Mark where platelets are.
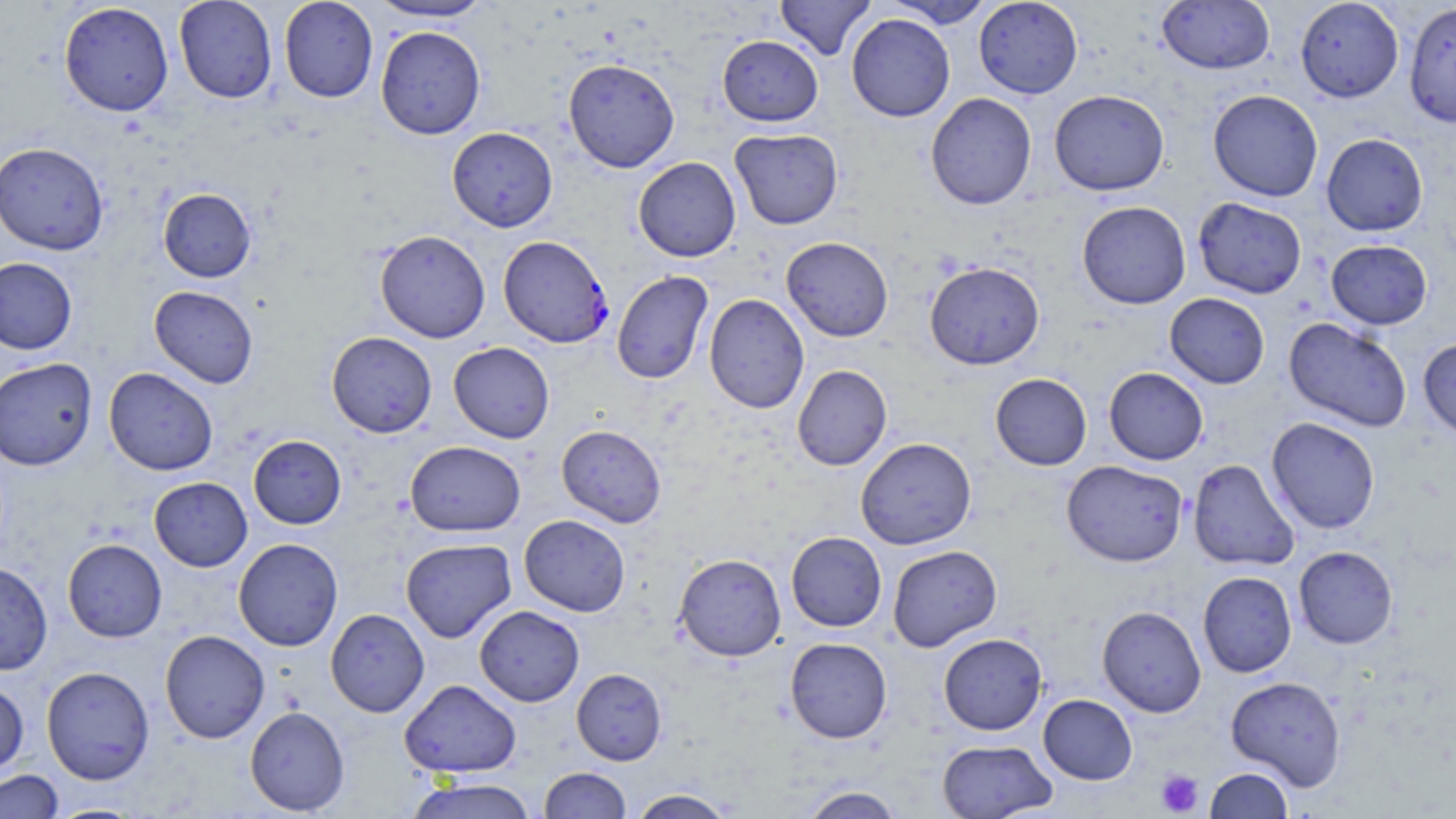

Approximate bounding boxes as (x1, y1, x2, y2) in pixels.
Platelets: (1155, 769, 1203, 816).

Plasmodium falciparum-infected red blood cell locations: (499, 236, 614, 350). Uninfected red blood cell locations: (174, 0, 277, 104), (278, 0, 378, 103), (775, 0, 876, 60), (973, 0, 1083, 98), (1295, 0, 1404, 103), (368, 1, 497, 23), (884, 1, 996, 27), (1157, 1, 1274, 75), (58, 2, 174, 117), (1404, 3, 1455, 128), (846, 13, 955, 122), (375, 26, 486, 139), (717, 35, 823, 126), (563, 58, 680, 172), (1049, 90, 1169, 195), (1208, 90, 1323, 202), (925, 92, 1037, 210), (447, 126, 558, 232), (730, 128, 843, 230), (1321, 133, 1429, 236), (0, 141, 109, 255), (633, 157, 741, 262), (158, 188, 256, 282), (1193, 197, 1307, 299), (1077, 201, 1191, 309), (375, 229, 490, 343), (781, 236, 893, 342), (1326, 240, 1432, 330), (0, 256, 78, 354), (924, 261, 1045, 370), (611, 270, 713, 384), (149, 285, 258, 389), (704, 293, 810, 413), (1165, 293, 1269, 389), (1283, 317, 1412, 432), (326, 332, 437, 437), (1418, 338, 1456, 440), (448, 342, 554, 443), (0, 357, 97, 471), (792, 364, 892, 471), (104, 367, 218, 476), (1104, 367, 1208, 465), (990, 373, 1092, 470), (1266, 417, 1380, 533), (556, 424, 666, 528), (248, 435, 346, 529), (856, 437, 977, 550), (405, 440, 525, 536), (1188, 459, 1300, 571), (1061, 460, 1188, 567), (149, 477, 252, 572), (519, 514, 630, 616), (786, 531, 887, 632), (233, 538, 343, 651), (62, 539, 167, 642), (401, 539, 517, 642), (887, 545, 1002, 652), (1293, 546, 1398, 649), (674, 553, 786, 661), (0, 561, 52, 675), (1197, 571, 1296, 677), (474, 605, 585, 706), (1097, 605, 1206, 717), (325, 608, 430, 717), (159, 630, 270, 743), (938, 632, 1048, 735), (785, 637, 892, 743), (41, 666, 154, 784), (571, 668, 667, 765), (1226, 676, 1347, 791), (399, 679, 521, 777), (0, 681, 29, 776), (1038, 694, 1137, 785), (245, 706, 350, 816), (936, 739, 1057, 818), (539, 767, 631, 818), (1204, 767, 1293, 818), (0, 769, 64, 818), (405, 777, 539, 819), (799, 786, 904, 818), (628, 788, 737, 819), (48, 803, 145, 818). Slide-level diagnosis: Plasmodium falciparum. 1000x magnification. May-Grünwald-Giemsa stain. Thin blood smear. Image is 1456×819 pixels. Light microscopy. Single field of view.